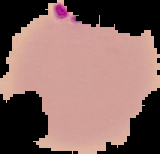
image type = segmented cell region on a black background
preparation = thin blood smear
image size = 160×154 pixels
result = Plasmodium parasites detected